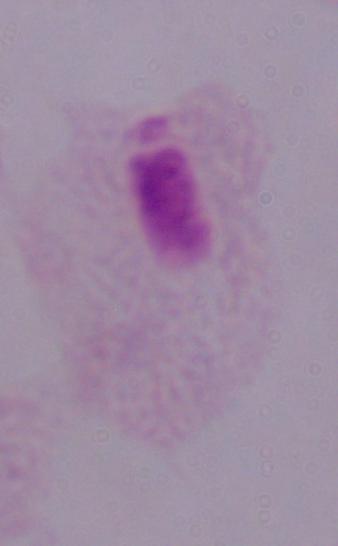
Summary:
  - Modality: photomicrograph
  - Magnification: 1000x
  - Identification: trichomonad